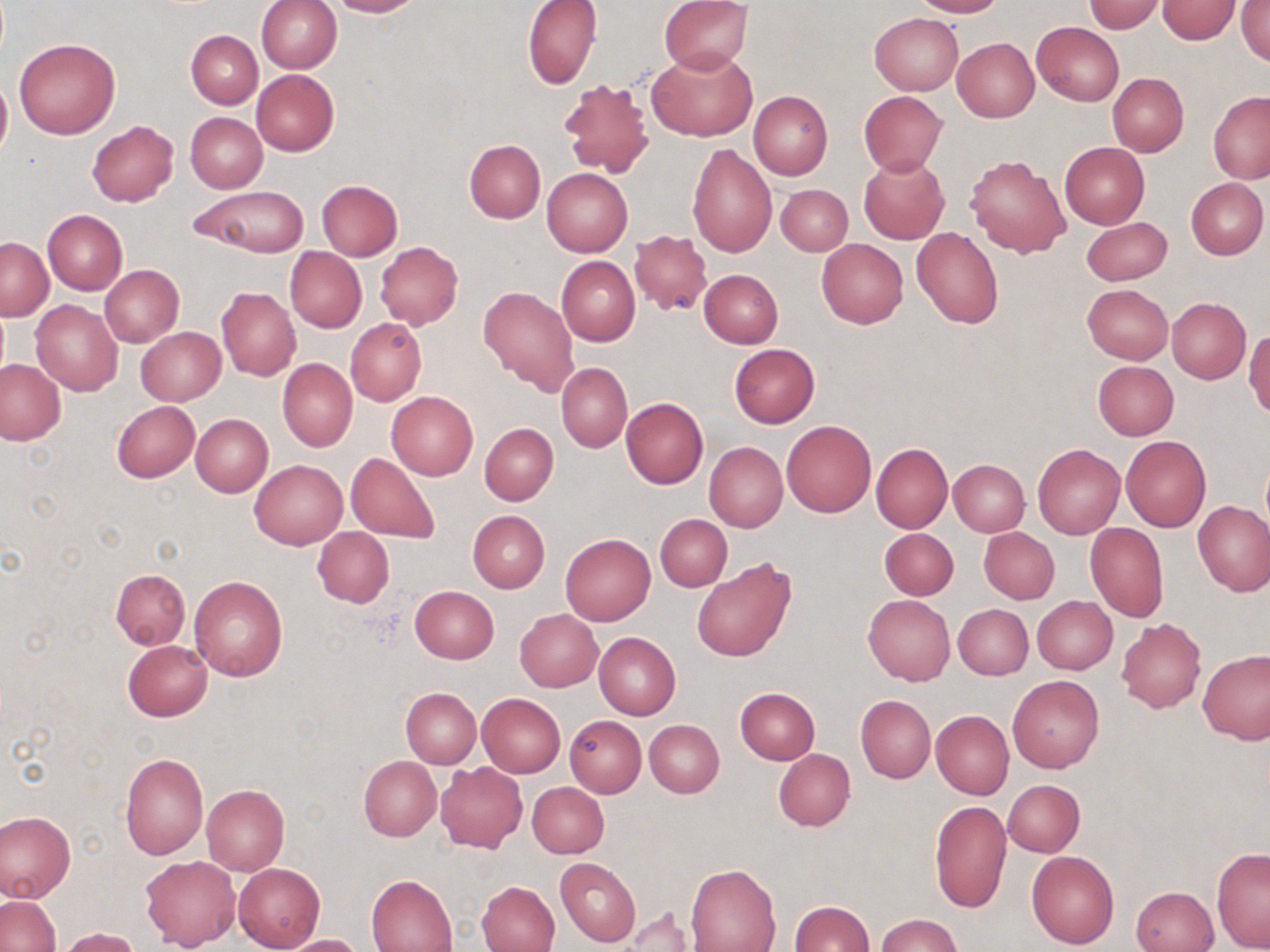

{
  "slide_level_diagnosis": "negative for blood parasites",
  "stain": "May-Grünwald-Giemsa",
  "image_size": "1270×952 pixels",
  "preparation": "thin blood smear",
  "magnification": "1000x",
  "uninfected_red_blood_cell_locations": "approximate bounding boxes as (x1,y1)-(x2,y2) corner pairs in pixels: (255,0)-(342,74), (327,0)-(420,17), (523,0)-(603,89), (660,0)-(752,72), (910,0)-(1004,17), (1156,1)-(1240,44), (1236,1)-(1270,67), (1083,2)-(1167,33), (869,12)-(963,94), (1030,21)-(1124,105), (186,30)-(263,108), (952,38)-(1040,123), (14,39)-(120,140), (649,48)-(757,141), (251,69)-(340,155), (1108,73)-(1188,156), (559,77)-(655,178), (0,78)-(11,158), (749,90)-(832,180), (859,91)-(947,176), (1209,91)-(1270,183), (185,112)-(267,192), (87,120)-(178,208), (464,140)-(545,223), (688,142)-(777,257), (1059,142)-(1150,228), (965,155)-(1070,258), (858,156)-(950,244), (541,169)-(633,256), (1186,177)-(1268,260), (316,180)-(402,260), (776,184)-(852,255), (192,186)-(309,257), (42,209)-(127,294), (1082,217)-(1171,285), (912,226)-(1004,329), (631,230)-(716,315), (1,237)-(52,320), (816,239)-(908,328), (375,242)-(462,330), (285,247)-(366,332), (557,256)-(640,347), (100,265)-(184,348), (699,269)-(783,347), (1082,283)-(1173,365), (479,285)-(579,398), (217,287)-(300,381), (1167,298)-(1250,383), (30,300)-(122,395), (346,318)-(426,406), (136,327)-(225,404), (1244,330)-(1270,419), (729,344)-(820,427), (0,359)-(68,446), (277,359)-(357,452), (1092,360)-(1178,440), (556,363)-(632,453), (386,391)-(478,480), (621,398)-(708,488), (111,401)-(200,482), (190,414)-(273,497), (782,421)-(876,517), (480,423)-(558,505), (1120,434)-(1211,532), (705,442)-(787,532), (870,442)-(952,533), (1033,444)-(1125,538), (346,453)-(440,543), (947,459)-(1030,536), (249,460)-(347,549), (1193,500)-(1270,595), (467,511)-(550,592), (655,514)-(732,591), (1085,522)-(1168,622), (311,527)-(393,607), (978,527)-(1060,604), (878,528)-(958,600), (560,533)-(655,626), (692,557)-(795,662), (110,568)-(190,650), (189,577)-(288,681), (410,586)-(499,663), (864,594)-(954,685), (1031,596)-(1118,674), (953,603)-(1033,679), (515,609)-(602,692), (1117,618)-(1206,712), (594,632)-(681,720), (123,640)-(213,721), (1197,651)-(1270,744), (1007,674)-(1103,773), (400,687)-(480,767), (735,687)-(820,764), (476,693)-(565,778), (855,694)-(935,783), (931,710)-(1014,800), (564,715)-(646,797), (645,720)-(725,797), (772,749)-(854,831), (119,752)-(209,859), (358,756)-(441,840), (435,763)-(527,853), (1003,779)-(1085,857), (527,782)-(609,858), (202,784)-(289,875), (929,800)-(1011,913), (0,811)-(75,903), (1211,848)-(1270,952), (1026,850)-(1120,949), (140,855)-(240,950), (555,857)-(641,946), (234,863)-(326,952), (686,863)-(781,952), (366,875)-(456,951), (476,880)-(560,952), (1130,886)-(1220,952), (1,896)-(59,952), (789,901)-(874,951), (623,908)-(698,951), (877,915)-(962,952), (56,927)-(140,952), (282,934)-(362,952)",
  "field_of_view": "one of a larger specimen",
  "modality": "light microscopy"
}